Assess this cell for malaria.
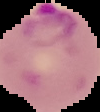

It is parasitized.

{
  "image_size": "100×112 pixels",
  "image_type": "segmented cell region with the area outside set to black",
  "preparation": "thin blood film"
}